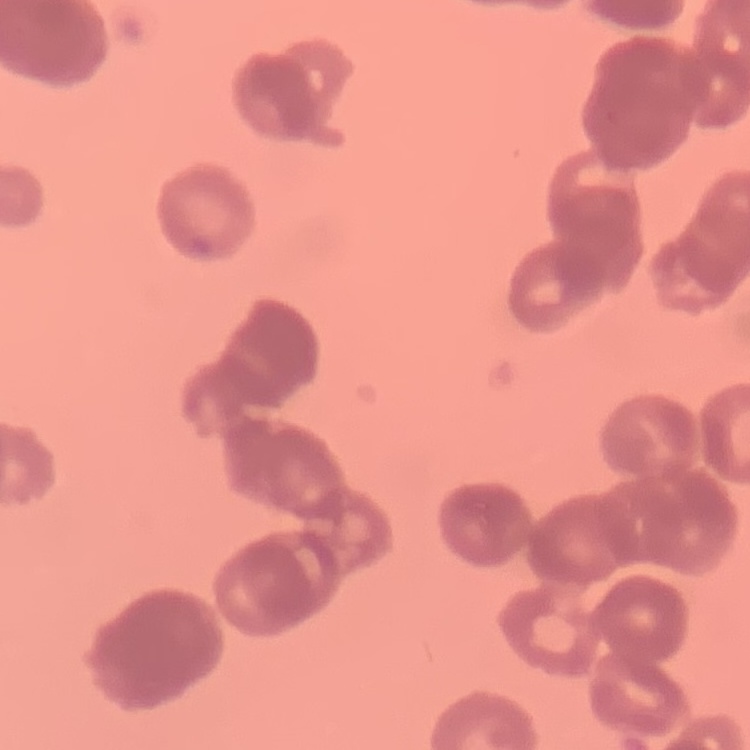
The erythrocytes exhibit rouleaux formation. Thin blood film. Square crop of a larger photomicrograph. Stained with either Field's or Giemsa.